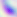
magnification = 400x
identification = Toxoplasma gondii
modality = micrograph